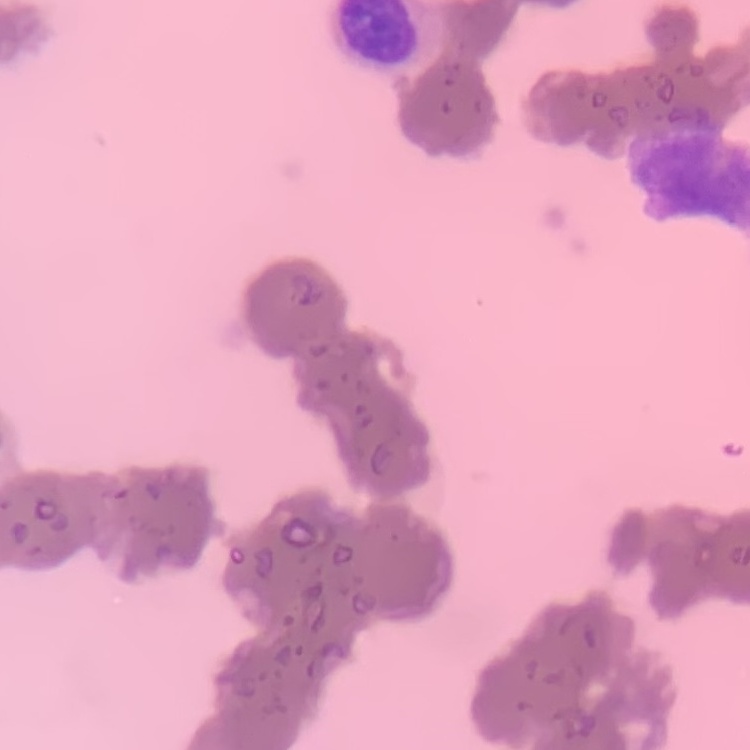
The erythrocytes show rouleaux formation. Thin blood smear. Field's or Giemsa stain. One tile cut from a larger photomicrograph.